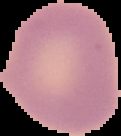

{
  "image_size": "121×136 pixels",
  "malaria_status": "uninfected",
  "image_type": "cell region segmented out of the field of view; surrounding area masked to black",
  "preparation": "thin blood smear"
}